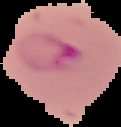
Summary:
  - Image size: 121×127 pixels
  - Result: malaria parasites detected
  - Preparation: thin blood film
  - Image type: cell region segmented out of the field of view; surrounding area masked to black